Name the parasite shown.
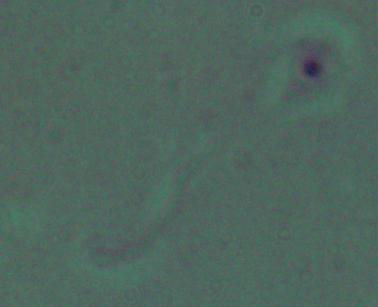

This is Leishmania.

1000x magnification. Micrograph.